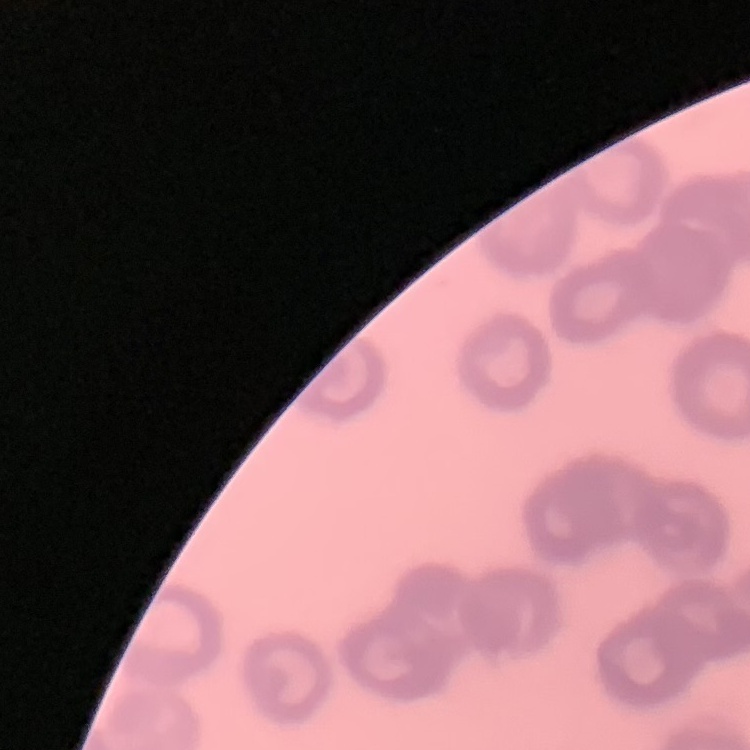 The red blood cells show rouleaux formation. Thin peripheral smear. Field's or Giemsa stain. Square crop of a larger photomicrograph.